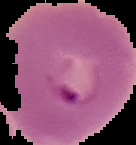

image type = segmented cell region with the area outside set to black
preparation = thin blood smear
image size = 136×145 pixels
result = malaria parasites identified